Locate every malaria parasite.
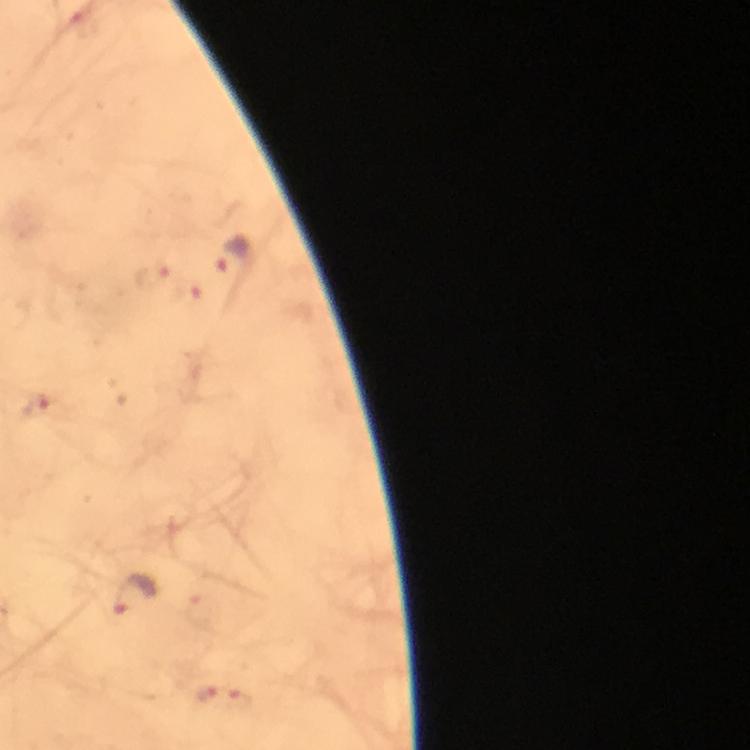
Approximate object centers, in pixels from the top-left corner.
Malaria parasites: (x=89, y=30), (x=234, y=254), (x=151, y=276), (x=38, y=407), (x=134, y=593), (x=224, y=698).

stain = Giemsa
capture = smartphone mounted on the microscope
magnification = 100x
cropped from = a single field of view
preparation = thick smear
image size = 750×750 pixels
context = from a diagnostic examination for malaria
immersion oil = applied